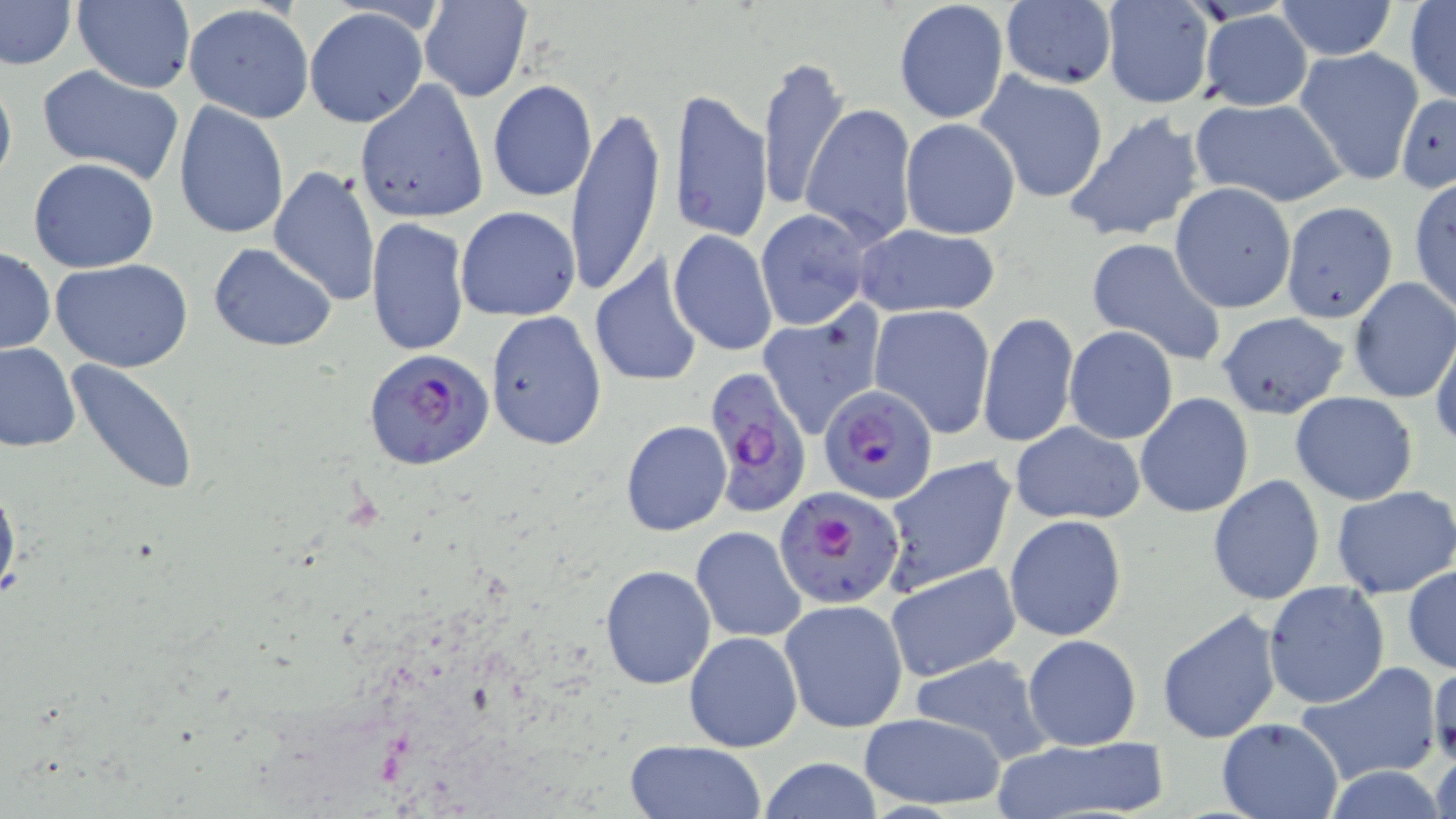
{
  "slide_level_diagnosis": "Plasmodium falciparum",
  "uninfected_red_blood_cell_locations": "approximate bounding boxes as (x1, y1, x2, y2) in pixels: (72, 0, 196, 93), (1275, 0, 1398, 60), (0, 1, 77, 70), (420, 1, 532, 101), (893, 1, 1010, 125), (998, 1, 1119, 90), (1099, 1, 1216, 109), (1404, 2, 1456, 107), (183, 5, 313, 123), (306, 8, 427, 128), (1199, 9, 1313, 111), (1296, 47, 1425, 186), (756, 54, 852, 215), (36, 63, 186, 185), (0, 68, 16, 197), (975, 71, 1110, 205), (354, 79, 489, 223), (487, 80, 598, 201), (670, 88, 771, 244), (1396, 94, 1456, 193), (1189, 97, 1348, 207), (565, 100, 663, 300), (174, 102, 290, 240), (802, 103, 919, 247), (1064, 110, 1206, 244), (898, 118, 1020, 239), (28, 157, 159, 273), (268, 165, 379, 306), (1409, 176, 1455, 314), (1170, 183, 1296, 312), (1281, 199, 1400, 322), (455, 207, 581, 321), (754, 208, 879, 330), (365, 218, 471, 361), (853, 224, 1003, 320), (668, 229, 778, 357), (1086, 237, 1228, 368), (209, 242, 338, 353), (0, 247, 55, 355), (587, 255, 704, 389), (50, 259, 194, 371), (1348, 277, 1456, 404), (868, 305, 996, 438), (758, 308, 887, 439), (485, 311, 607, 451), (1215, 311, 1350, 419), (978, 313, 1079, 448), (1065, 326, 1178, 444), (1430, 328, 1456, 452), (0, 340, 80, 451), (66, 360, 200, 496), (1290, 392, 1420, 506), (1135, 393, 1254, 518), (621, 420, 732, 537), (1009, 422, 1147, 525), (881, 456, 1015, 594), (0, 473, 20, 608), (1207, 475, 1326, 607), (1331, 486, 1456, 599), (1004, 515, 1127, 641), (689, 526, 807, 643), (621, 542, 794, 670), (884, 562, 1021, 683), (599, 563, 716, 690), (1403, 564, 1456, 674), (1263, 581, 1390, 709), (779, 598, 908, 734), (1157, 608, 1285, 745), (684, 631, 801, 752), (1022, 634, 1142, 751), (907, 654, 1054, 766), (1429, 657, 1456, 770), (1296, 662, 1444, 785), (857, 712, 1009, 811), (1215, 717, 1346, 819), (992, 735, 1169, 819), (623, 739, 768, 819), (1431, 746, 1456, 819), (758, 756, 884, 819), (1321, 767, 1448, 819)",
  "preparation": "thin blood film",
  "field_of_view": "one of a larger specimen",
  "modality": "light microscopy",
  "magnification": "1000x",
  "stain": "May-Grünwald-Giemsa",
  "plasmodium_falciparum_infected_red_blood_cell_locations": "approximate bounding boxes as (x1, y1, x2, y2) in pixels: (364, 346, 495, 472), (705, 371, 812, 516), (819, 381, 942, 506), (774, 485, 907, 609)",
  "image_size": "1456×819 pixels"
}